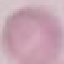

result = negative for malaria parasites
stain = Giemsa
preparation = thin blood film
capture = smartphone camera at the microscope eyepiece
image type = cell patch, automatically extracted from a larger field of view and resized to 64 × 64 pixels